Assess the morphology of the red blood cells.
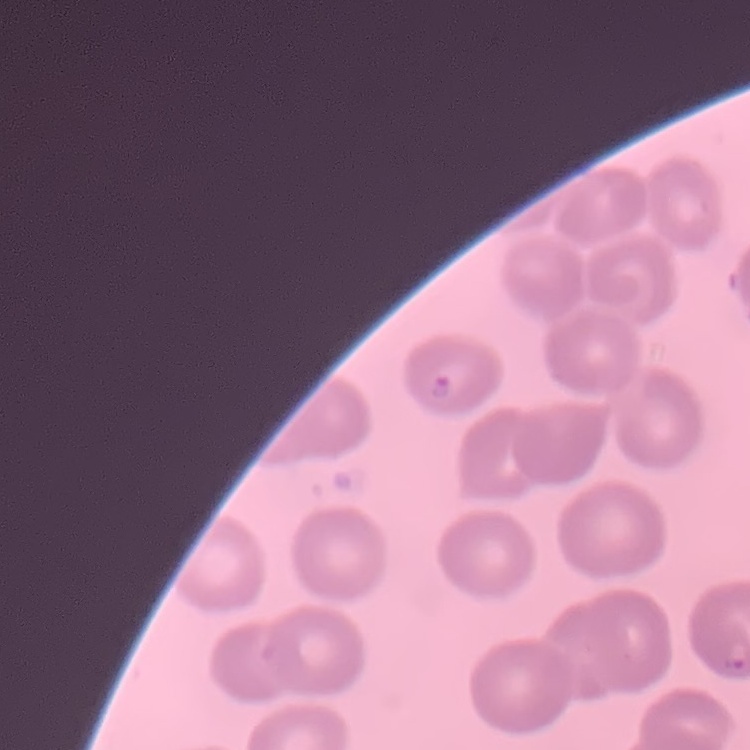
They show no rouleaux formation.

Summary:
  - Stain: Field's or Giemsa
  - Preparation: thin blood smear
  - Image type: square crop of a larger photomicrograph